Identify the parasite.
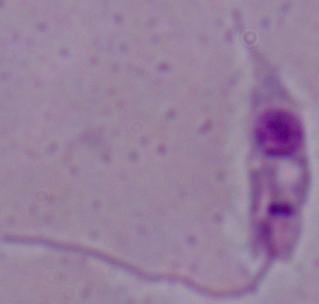
Leishmania.

Micrograph. 1000x magnification.